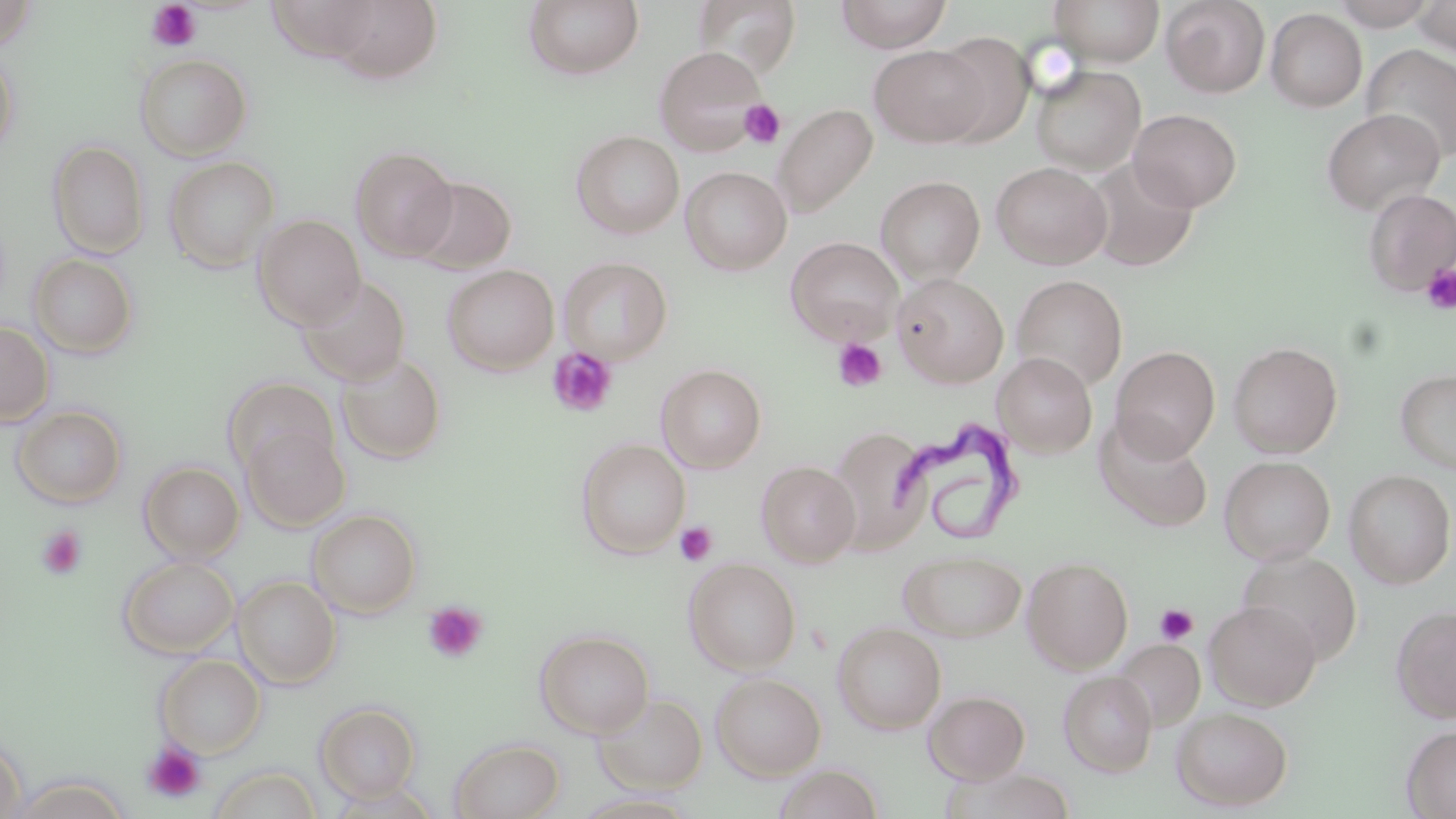

Summary:
  - Coordinate format: approximate bounding boxes as [x1, y1, x2, y2] in pixels
  - Uninfected red blood cell locations: [0, 0, 38, 49], [524, 0, 644, 80], [835, 0, 953, 52], [1050, 0, 1164, 66], [1160, 0, 1270, 97], [1327, 0, 1442, 29], [1412, 0, 1456, 58], [693, 1, 802, 79], [323, 2, 443, 83], [1266, 9, 1367, 111], [932, 32, 1035, 147], [1360, 44, 1456, 161], [869, 45, 990, 147], [654, 46, 768, 155], [0, 47, 19, 158], [134, 53, 252, 161], [1030, 65, 1146, 175], [772, 104, 878, 217], [1321, 108, 1444, 216], [1129, 109, 1241, 211], [571, 130, 684, 238], [47, 140, 150, 259], [350, 146, 459, 261], [163, 156, 280, 273], [1085, 158, 1198, 271], [991, 162, 1112, 270], [680, 166, 792, 275], [408, 176, 516, 274], [876, 176, 985, 284], [1363, 188, 1456, 296], [252, 214, 366, 329], [786, 237, 904, 344], [28, 253, 138, 358], [558, 256, 673, 365], [442, 264, 559, 375], [893, 274, 1009, 387], [1011, 274, 1128, 390], [297, 276, 411, 386], [0, 321, 54, 427], [1227, 340, 1343, 457], [1111, 345, 1220, 460], [993, 352, 1097, 457], [336, 353, 447, 465], [656, 364, 767, 472], [1395, 368, 1456, 475], [223, 377, 339, 477], [11, 405, 127, 509], [1095, 417, 1213, 532], [241, 423, 349, 532], [828, 426, 933, 554], [576, 439, 690, 558], [1219, 455, 1335, 565], [756, 460, 861, 567], [139, 461, 244, 562], [1343, 469, 1456, 588], [308, 509, 421, 618], [898, 549, 1027, 642], [1237, 550, 1362, 664], [118, 556, 239, 658], [1022, 556, 1134, 673], [684, 557, 801, 675], [233, 575, 342, 689], [1204, 600, 1321, 710], [1392, 604, 1456, 723], [831, 621, 947, 734], [535, 629, 654, 738], [1112, 639, 1205, 730], [155, 654, 266, 757], [1059, 670, 1157, 776], [710, 672, 826, 780], [924, 690, 1031, 784], [594, 693, 708, 794], [315, 702, 421, 802], [1171, 706, 1293, 811], [1402, 724, 1456, 818], [0, 737, 26, 819], [449, 738, 565, 819], [773, 764, 884, 819], [210, 766, 322, 819], [9, 776, 132, 819]
  - Platelet locations: [145, 1, 202, 52], [739, 100, 785, 148], [1420, 263, 1456, 314], [832, 338, 887, 393], [546, 346, 619, 418], [674, 522, 717, 566], [35, 525, 87, 582], [422, 601, 488, 664], [1154, 603, 1199, 646], [142, 741, 207, 804]
  - Trypanosoma brucei locations: [889, 418, 1024, 548]
  - Slide-level diagnosis: Trypanosoma brucei
  - Image size: 1456×819 pixels
  - Stain: May-Grünwald-Giemsa
  - Magnification: 1000x
  - Modality: light microscopy
  - Preparation: thin blood film
  - Field of view: single